State the preparation type.
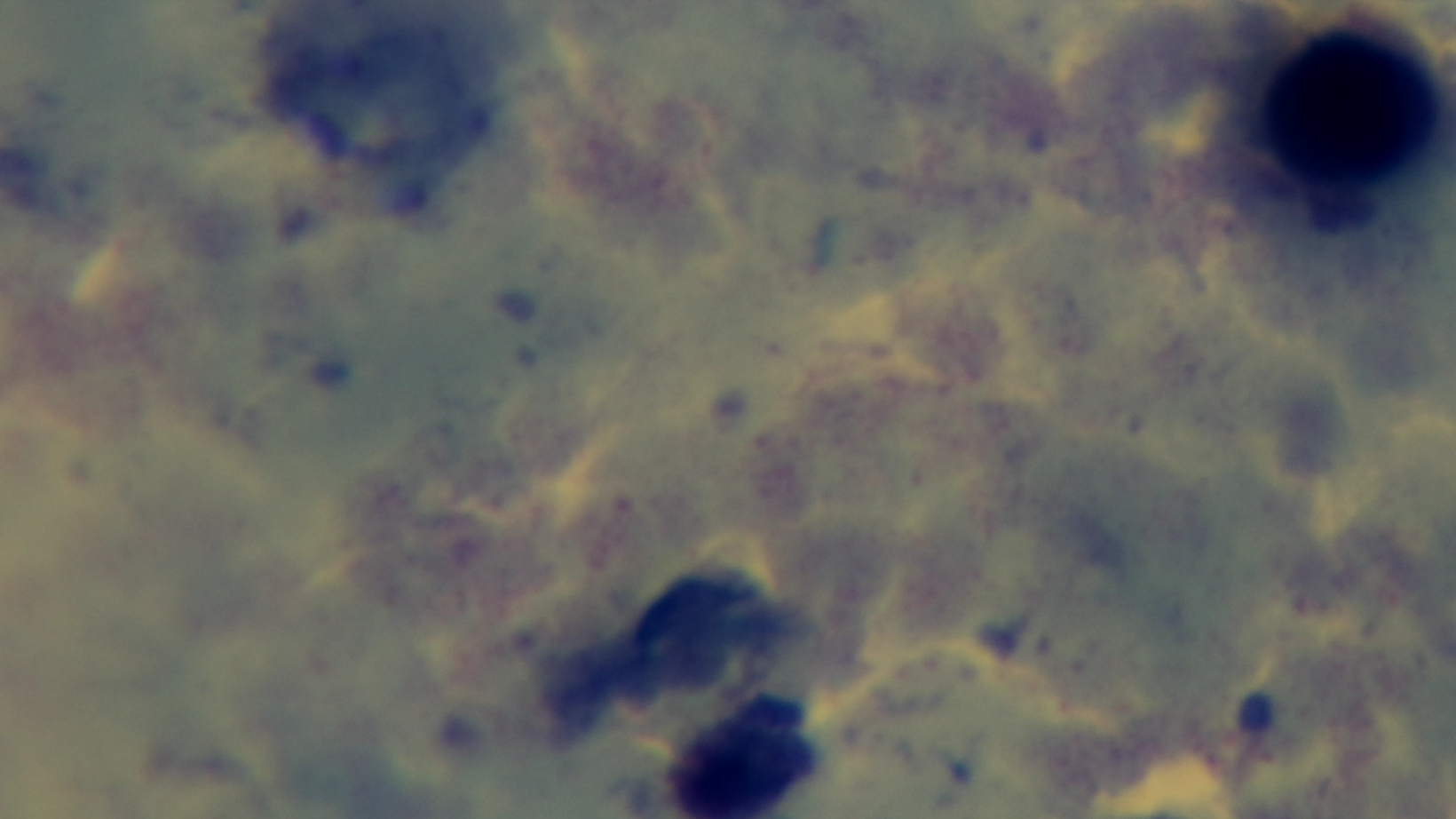
Thick.

Malaria status: uninfected. One field from the slide. Giemsa stain. Photomicrograph. Captured with a mounted 4K digital camera. 100x oil-immersion objective.